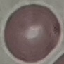
Summary:
  - Result: no malaria parasites seen
  - Image type: automatically extracted cell patch, resized to 64 × 64 pixels
  - Capture: smartphone camera at the microscope eyepiece
  - Stain: Giemsa
  - Preparation: thin blood film